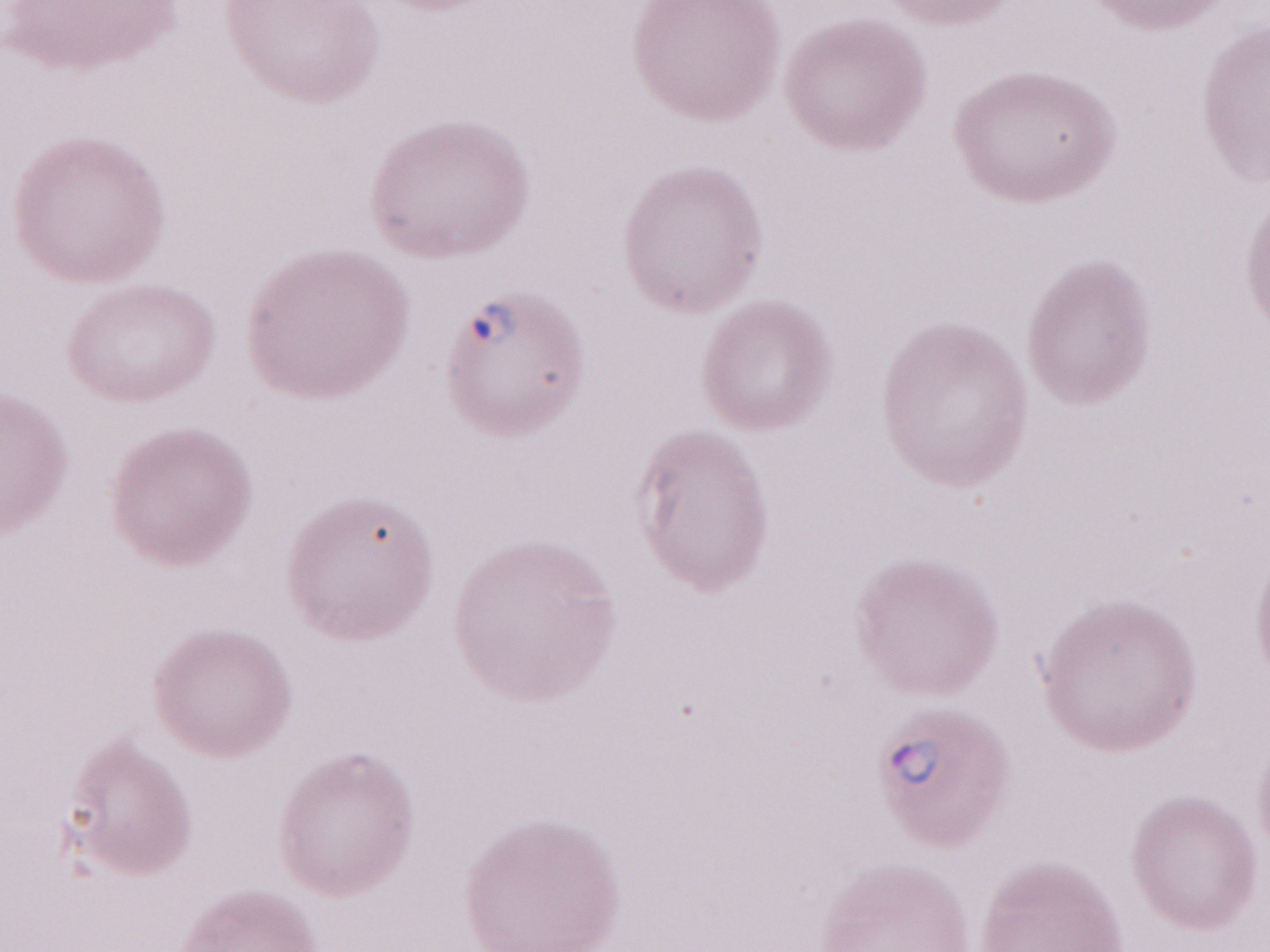

Image is 1270×952 pixels. Thin blood film. One field of this slide. Magnification: 1,000x. Patient diagnosis: malaria infection. May-Grünwald-Giemsa-stained preparation. Olympus BX43 microscope and DP73 digital camera.